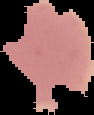

preparation = thin blood film
image size = 94×115 pixels
malaria status = uninfected
image type = segmented cell region on a black background